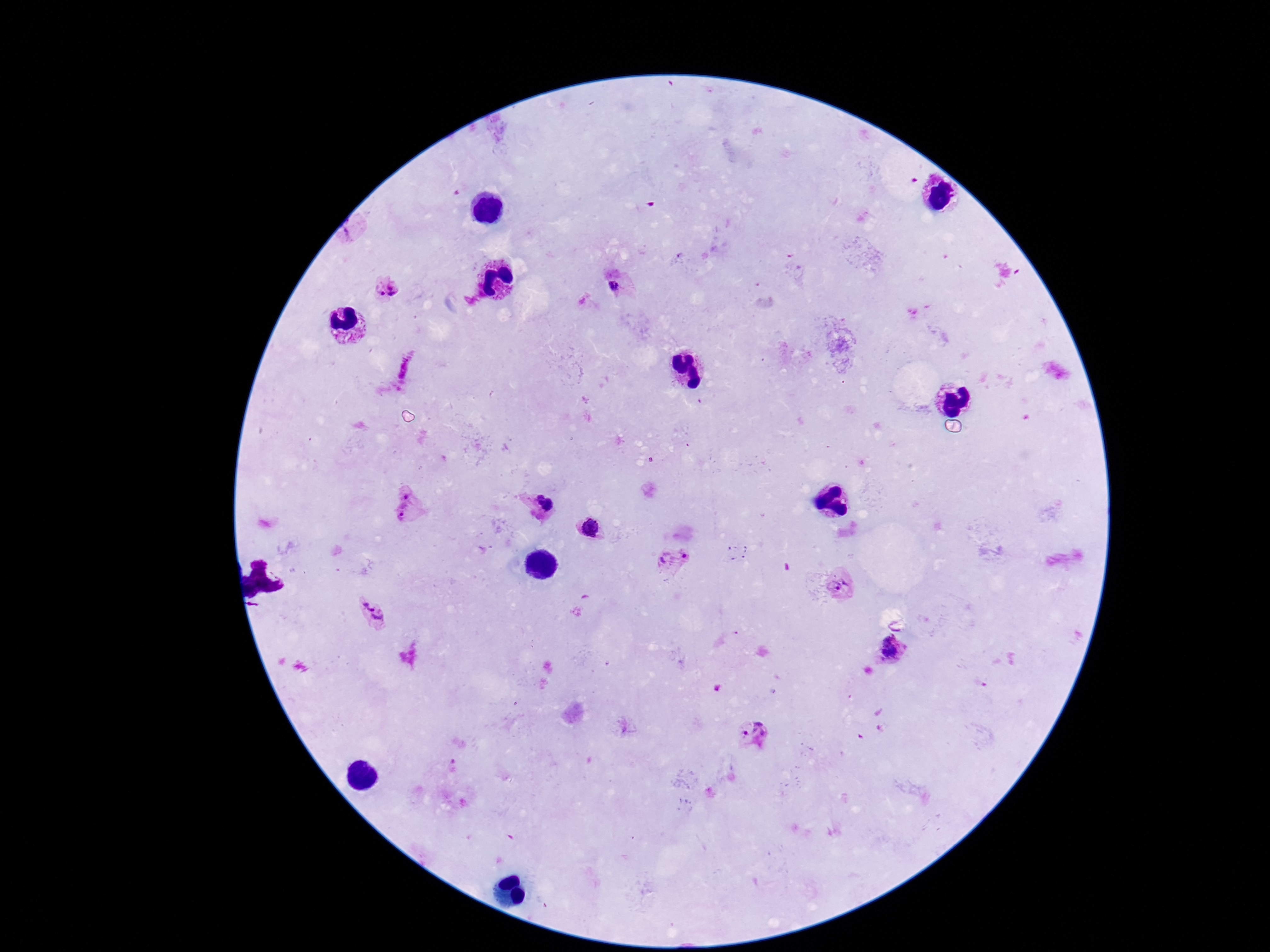

{
  "field_of_view": "one from this slide",
  "magnification": "100x",
  "capture": "smartphone camera through the microscope eyepiece",
  "image_size": "1270×952 pixels",
  "preparation": "thick blood smear",
  "stain": "Giemsa",
  "patient_malaria_status": "infected",
  "plasmodium_parasite_locations": "approximate centers as [x, y] in pixels: [613, 286], [387, 291], [407, 492], [539, 496], [547, 505], [407, 514], [590, 526], [675, 558], [840, 586], [372, 611], [892, 650], [760, 729], [745, 733]"
}